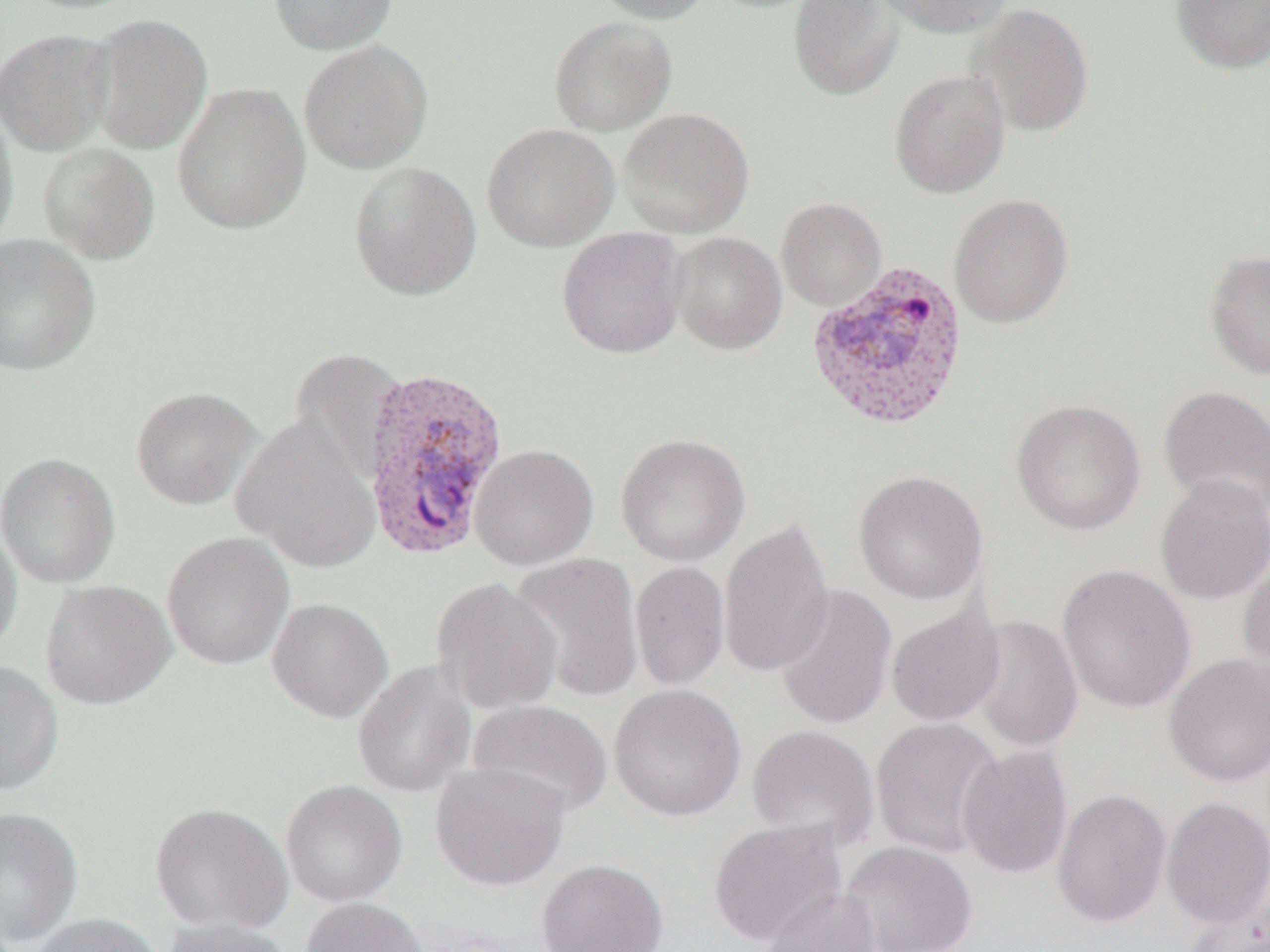

Approximate bounding boxes as named x1/y1/x2/y2 corners in pixels. Uninfected red blood cell locations: (x1=13, y1=0, x2=151, y2=14), (x1=269, y1=0, x2=398, y2=56), (x1=590, y1=0, x2=711, y2=24), (x1=787, y1=0, x2=905, y2=102), (x1=878, y1=0, x2=1014, y2=38), (x1=1171, y1=0, x2=1270, y2=75), (x1=965, y1=3, x2=1094, y2=138), (x1=85, y1=13, x2=213, y2=155), (x1=549, y1=16, x2=677, y2=136), (x1=0, y1=27, x2=116, y2=156), (x1=298, y1=39, x2=434, y2=175), (x1=889, y1=70, x2=1011, y2=199), (x1=172, y1=82, x2=313, y2=235), (x1=0, y1=103, x2=18, y2=252), (x1=618, y1=108, x2=754, y2=238), (x1=482, y1=123, x2=620, y2=252), (x1=38, y1=142, x2=161, y2=265), (x1=348, y1=161, x2=482, y2=301), (x1=949, y1=193, x2=1073, y2=328), (x1=776, y1=198, x2=886, y2=311), (x1=556, y1=227, x2=688, y2=359), (x1=669, y1=232, x2=788, y2=354), (x1=0, y1=233, x2=101, y2=376), (x1=1205, y1=251, x2=1270, y2=380), (x1=288, y1=347, x2=408, y2=479), (x1=1159, y1=384, x2=1270, y2=519), (x1=129, y1=385, x2=262, y2=510), (x1=1011, y1=399, x2=1145, y2=535), (x1=233, y1=416, x2=382, y2=573), (x1=615, y1=433, x2=751, y2=567), (x1=469, y1=443, x2=598, y2=569), (x1=0, y1=451, x2=120, y2=588), (x1=853, y1=469, x2=988, y2=604), (x1=1155, y1=473, x2=1270, y2=605), (x1=718, y1=518, x2=835, y2=678), (x1=0, y1=521, x2=22, y2=657), (x1=161, y1=531, x2=294, y2=670), (x1=509, y1=552, x2=644, y2=703), (x1=1238, y1=556, x2=1270, y2=683), (x1=629, y1=560, x2=730, y2=691), (x1=1057, y1=564, x2=1196, y2=713), (x1=431, y1=577, x2=564, y2=714), (x1=40, y1=579, x2=176, y2=710), (x1=774, y1=583, x2=898, y2=731), (x1=267, y1=597, x2=393, y2=722), (x1=886, y1=606, x2=1005, y2=727), (x1=968, y1=615, x2=1084, y2=753), (x1=1163, y1=653, x2=1270, y2=787), (x1=0, y1=661, x2=64, y2=796), (x1=352, y1=661, x2=477, y2=797), (x1=608, y1=683, x2=746, y2=821), (x1=467, y1=698, x2=613, y2=818), (x1=870, y1=717, x2=1004, y2=858), (x1=747, y1=725, x2=880, y2=850), (x1=957, y1=745, x2=1073, y2=879), (x1=430, y1=762, x2=571, y2=891), (x1=281, y1=779, x2=408, y2=907), (x1=1052, y1=788, x2=1171, y2=928), (x1=1162, y1=797, x2=1270, y2=927), (x1=149, y1=802, x2=293, y2=934), (x1=0, y1=807, x2=83, y2=947), (x1=709, y1=819, x2=847, y2=945), (x1=840, y1=841, x2=977, y2=952), (x1=536, y1=858, x2=668, y2=952), (x1=761, y1=885, x2=882, y2=952), (x1=1184, y1=893, x2=1270, y2=952), (x1=300, y1=897, x2=428, y2=952), (x1=29, y1=913, x2=162, y2=952), (x1=158, y1=918, x2=294, y2=952). Plasmodium vivax-infected red blood cell locations: (x1=810, y1=263, x2=973, y2=433), (x1=360, y1=364, x2=510, y2=562). Slide-level diagnosis: Plasmodium vivax. 1000x magnification. Single field of view. Thin blood smear. Optical microscopy. Image is 1270×952 pixels.